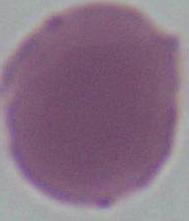
modality: photomicrograph
identification: erythrocyte
magnification: 1000x